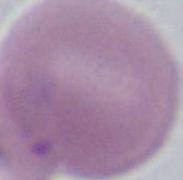
Summary:
  - Magnification: 1000x
  - Modality: micrograph
  - Identification: red blood cell